State which parasite is depicted.
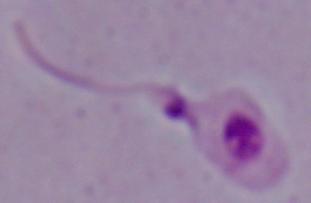

This is Leishmania.

modality: photomicrograph
magnification: 1000x